State which cell type is depicted.
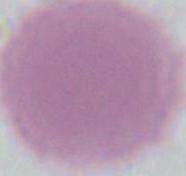
This is an erythrocyte.

1000x magnification. Photomicrograph.